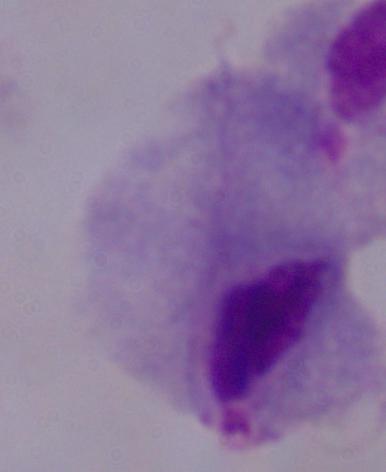 1000x magnification. Micrograph. A trichomonad is seen.